Identify the parasite.
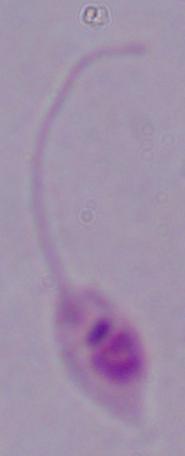

Leishmania.

Summary:
  - Modality: photomicrograph
  - Magnification: 1000x